Identify the parasite.
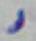

Toxoplasma gondii.

Photomicrograph. 1000x magnification.